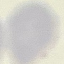

{
  "malaria_status": "uninfected",
  "preparation": "thin blood smear",
  "image_type": "automatically extracted cell patch, resized to 64 × 64 pixels",
  "capture": "smartphone camera at the microscope eyepiece",
  "stain": "Giemsa"
}